Describe the morphology of the erythrocytes.
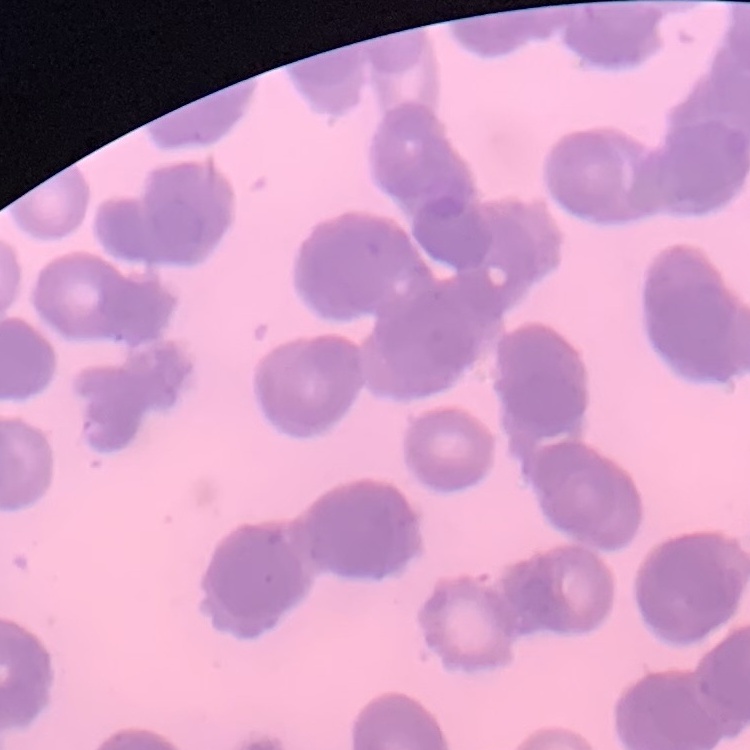
Rouleaux formation.

Field's or Giemsa stain. One tile cut from a larger photomicrograph. Thin blood film.